Report the malaria status of this cell.
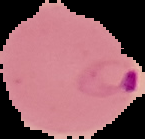

Parasitized.

Summary:
  - Preparation: thin blood film
  - Image type: segmented cell region with the area outside set to black
  - Image size: 145×139 pixels